Classify this cell by malaria status.
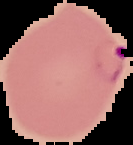

It is parasitized.

Summary:
  - Image type: cell region segmented out of the field of view; surrounding area masked to black
  - Preparation: thin blood smear
  - Image size: 133×145 pixels